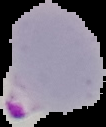

Malaria status: parasitized. From a thin blood film. Image is 106×127 pixels. Cell region segmented out of the field of view; the surrounding area is masked to black.